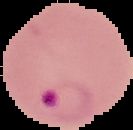
{
  "preparation": "thin blood smear",
  "image_size": "133×130 pixels",
  "result": "malaria parasites identified",
  "image_type": "segmented cell region with the area outside set to black"
}